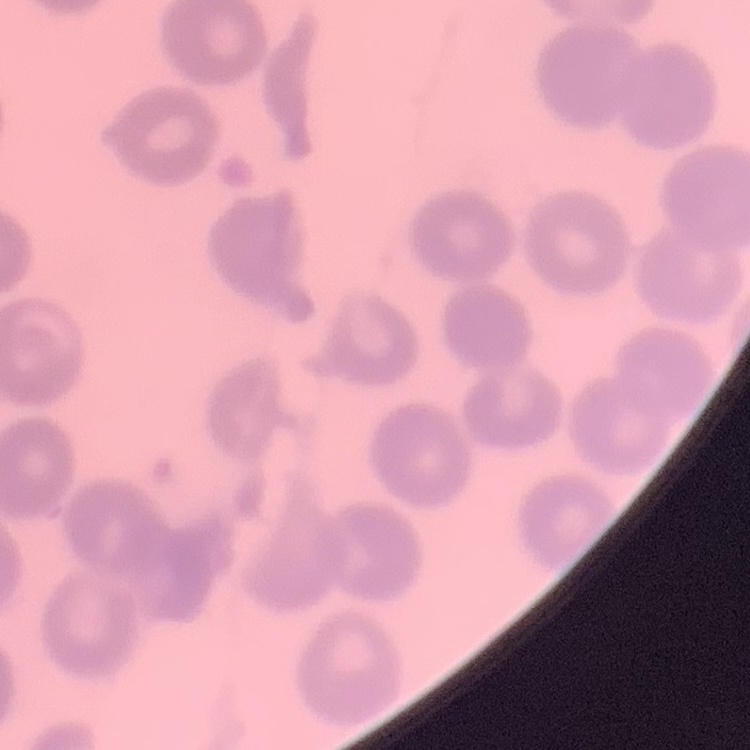
red blood cell morphology = no rouleaux formation
image type = square crop of a larger photomicrograph
stain = Field's or Giemsa
preparation = thin blood film